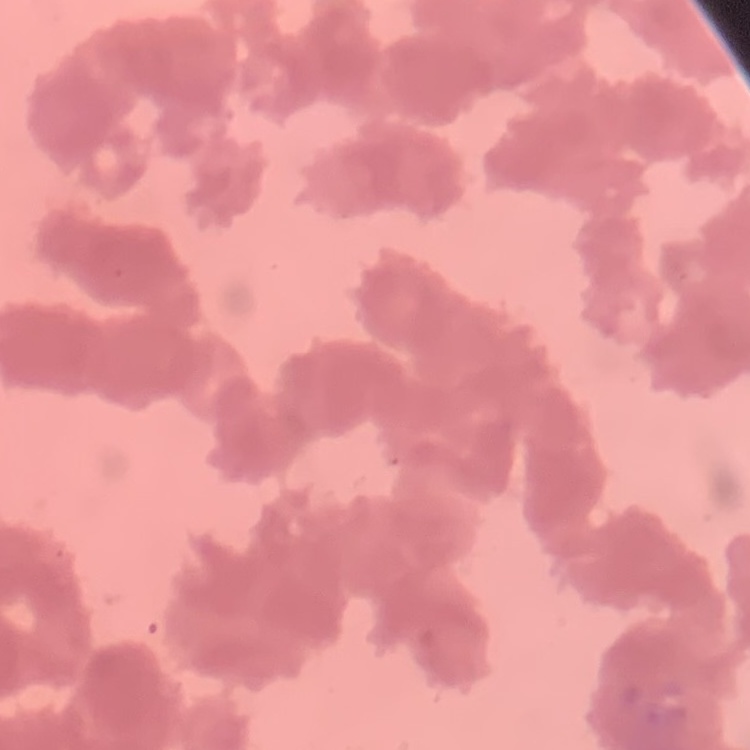
red_blood_cell_morphology: rouleaux formation
preparation: thin peripheral smear
image_type: one tile cut from a larger photomicrograph
stain: Field's or Giemsa